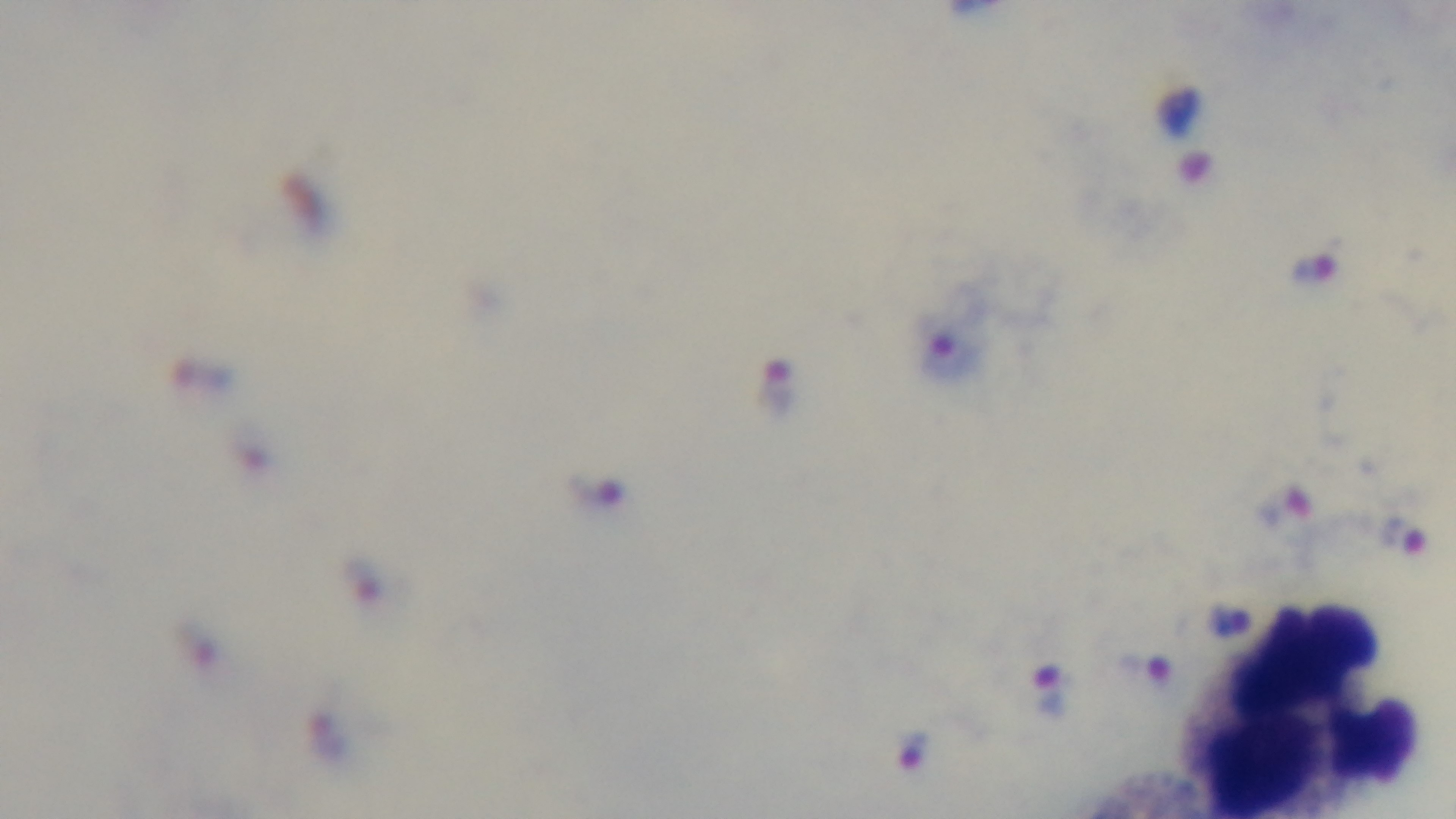 Light microscopy. Oil-immersion objective, 100x. Captured with a mounted 4K digital camera. Single field of view. Malaria status: infected. Giemsa-stained. Preparation: thick smear.